Name the blood parasite species.
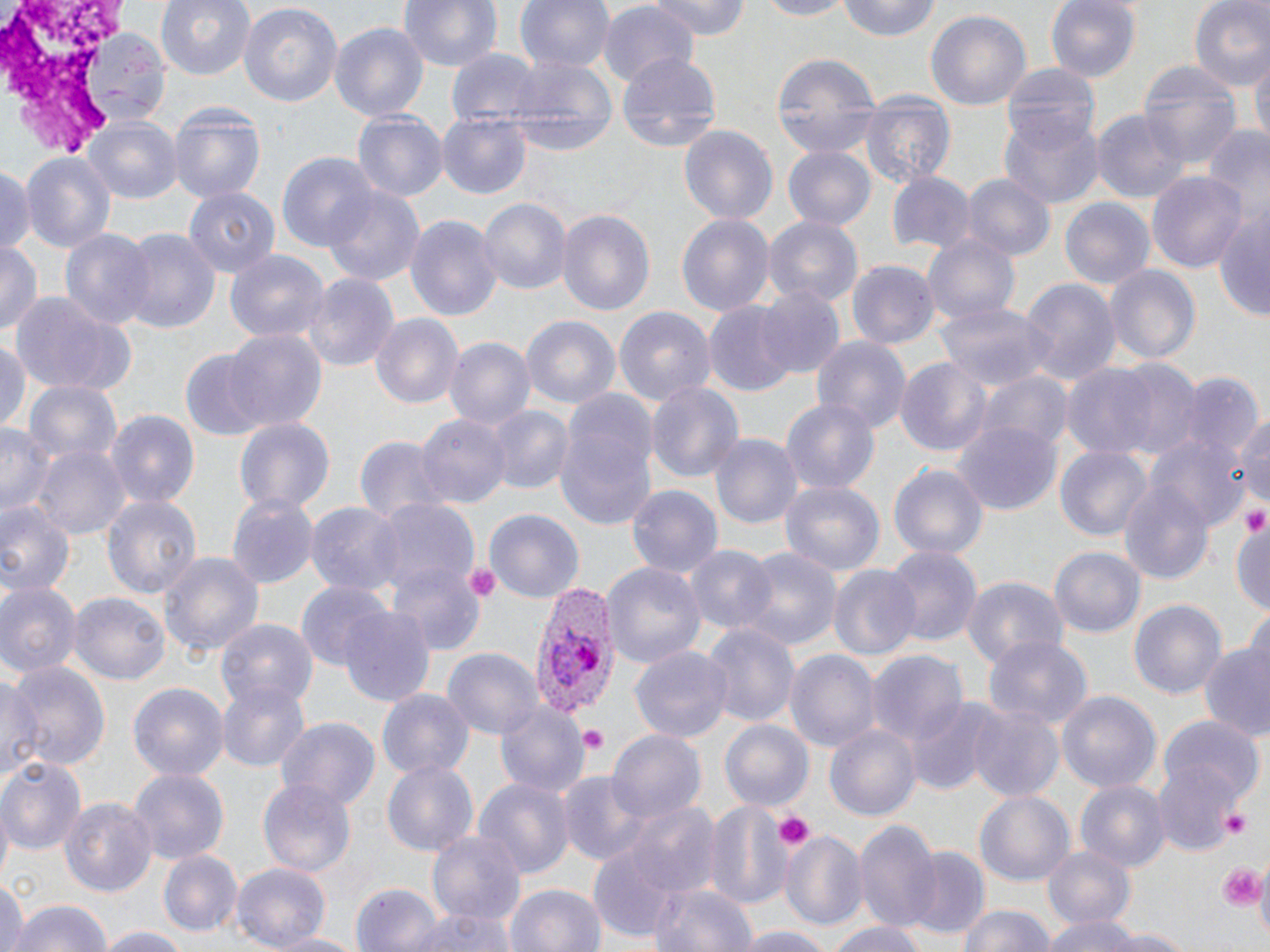

Plasmodium vivax.

Approximate bounding boxes as (x1,y1)-(x2,y2) corner pairs in pixels. Platelet locations: (1242,508)-(1268,535), (460,561)-(501,603), (576,726)-(606,752), (1222,805)-(1254,840), (775,810)-(814,851), (1219,862)-(1266,911), (1252,866)-(1270,934). Plasmodium vivax-infected red blood cell locations: (531,585)-(619,719). Uninfected red blood cell locations: (155,0)-(256,81), (397,0)-(504,77), (515,0)-(613,76), (643,0)-(754,41), (749,0)-(856,20), (834,0)-(943,43), (1045,0)-(1143,85), (1189,0)-(1270,93), (239,2)-(342,110), (597,3)-(700,89), (926,9)-(1031,114), (330,21)-(432,123), (81,29)-(166,122), (446,50)-(540,127), (770,50)-(880,160), (615,52)-(722,153), (1251,52)-(1269,157), (504,57)-(618,160), (1000,62)-(1101,146), (1139,63)-(1238,165), (861,93)-(955,189), (166,100)-(267,207), (1094,108)-(1189,205), (354,110)-(447,202), (437,111)-(531,200), (1001,113)-(1103,207), (83,115)-(182,202), (677,124)-(778,225), (1202,124)-(1269,219), (782,145)-(876,231), (20,151)-(117,259), (278,152)-(378,257), (0,164)-(34,257), (1149,169)-(1249,272), (888,171)-(975,254), (961,173)-(1055,262), (321,183)-(428,290), (183,189)-(278,279), (479,197)-(571,297), (1058,197)-(1155,294), (555,206)-(654,318), (1214,206)-(1269,323), (405,213)-(502,325), (675,213)-(775,323), (765,217)-(863,310), (119,226)-(220,338), (59,229)-(155,332), (925,233)-(1020,328), (0,240)-(41,338), (226,249)-(327,345), (847,261)-(937,349), (1105,265)-(1199,366), (301,273)-(400,373), (1019,278)-(1121,389), (755,284)-(847,380), (9,294)-(129,395), (934,299)-(1049,390), (705,303)-(795,396), (614,306)-(716,411), (370,314)-(465,411), (520,315)-(622,413), (223,328)-(327,432), (811,333)-(912,435), (445,337)-(534,430), (0,340)-(29,434), (181,353)-(266,441), (894,356)-(993,457), (1103,359)-(1203,461), (1058,362)-(1169,458), (1179,372)-(1260,468), (978,374)-(1072,459), (645,380)-(745,485), (24,381)-(121,470), (554,392)-(658,530), (781,397)-(881,495), (1232,404)-(1269,507), (486,405)-(574,496), (105,409)-(198,506), (418,415)-(511,509), (231,416)-(336,516), (954,421)-(1061,512), (0,423)-(51,521), (355,434)-(446,528), (709,434)-(801,532), (1150,436)-(1249,533), (1055,443)-(1152,541), (35,448)-(127,539), (891,463)-(988,563), (1119,478)-(1214,589), (778,479)-(885,576), (628,484)-(720,581), (102,492)-(202,602), (227,496)-(318,587), (374,499)-(480,600), (306,502)-(406,600), (0,503)-(76,599), (483,509)-(583,604), (1230,512)-(1270,621), (684,544)-(775,636), (882,545)-(981,653), (1051,547)-(1143,640), (734,548)-(842,655), (158,550)-(266,661), (603,562)-(706,670), (388,566)-(484,654), (829,566)-(921,662), (960,575)-(1068,670), (0,580)-(81,679), (295,581)-(391,671), (70,591)-(170,686), (1128,598)-(1227,702), (339,607)-(435,708), (218,620)-(316,710), (703,623)-(800,731), (984,637)-(1091,729), (1199,642)-(1270,740), (630,646)-(733,743), (784,647)-(880,751), (442,648)-(545,740), (866,648)-(967,749), (6,660)-(112,772), (1,670)-(45,787), (216,680)-(309,772), (128,683)-(229,782), (377,689)-(476,781), (1055,691)-(1161,797), (493,699)-(587,797), (907,699)-(993,794), (966,702)-(1064,801), (1161,716)-(1263,803), (275,718)-(379,811), (718,719)-(814,811), (825,723)-(922,822), (609,729)-(706,822), (0,757)-(85,855), (1154,757)-(1244,855), (382,761)-(477,856), (129,769)-(229,862), (559,772)-(658,867), (474,777)-(574,878), (258,779)-(356,876), (1076,780)-(1169,871), (975,791)-(1074,887), (59,797)-(158,897), (704,797)-(798,911), (617,799)-(718,896), (853,819)-(942,934), (427,829)-(529,925), (779,829)-(867,933), (1043,844)-(1136,931), (585,847)-(688,943), (157,849)-(242,937), (905,850)-(988,942), (231,863)-(332,950), (0,876)-(25,952), (648,880)-(757,952), (353,882)-(442,952), (503,882)-(606,952), (6,899)-(112,952), (405,904)-(515,952), (957,905)-(1057,952), (1044,915)-(1150,952), (830,922)-(929,952), (729,925)-(840,952), (97,926)-(188,952), (1092,927)-(1194,952), (268,930)-(363,952). Thin blood film. Image is 1270×952 pixels. One field of a larger specimen. Light microscopy. Captured at 1000x magnification. May-Grünwald-Giemsa stain.